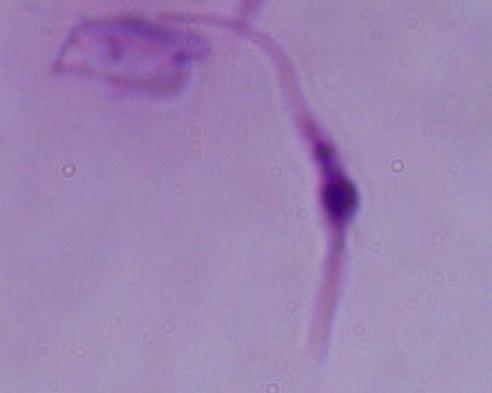

identification = Leishmania
magnification = 1000x
modality = photomicrograph